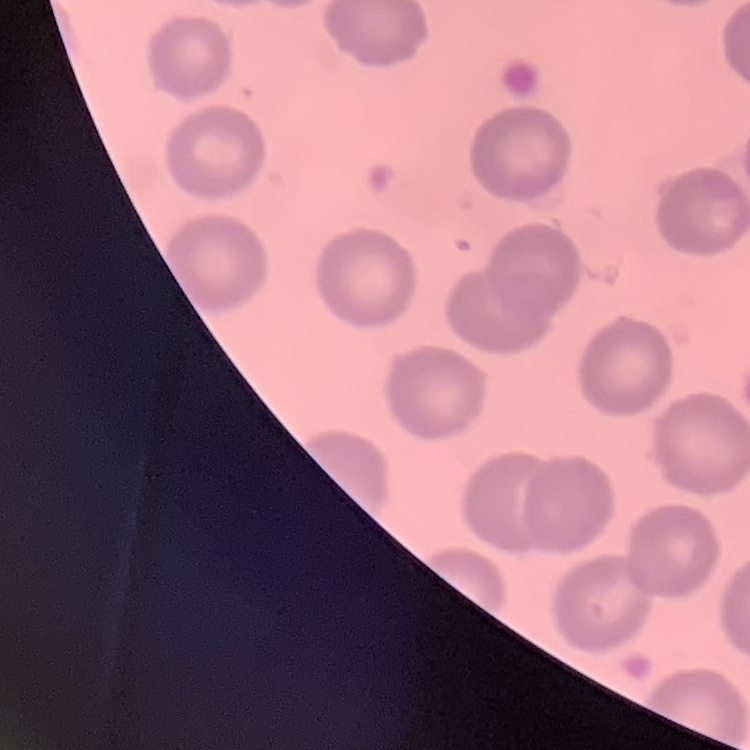

erythrocyte morphology = no rouleaux formation
stain = Field's or Giemsa
image type = square crop of a larger photomicrograph
preparation = thin blood film